Outline each Trypanosoma brucei.
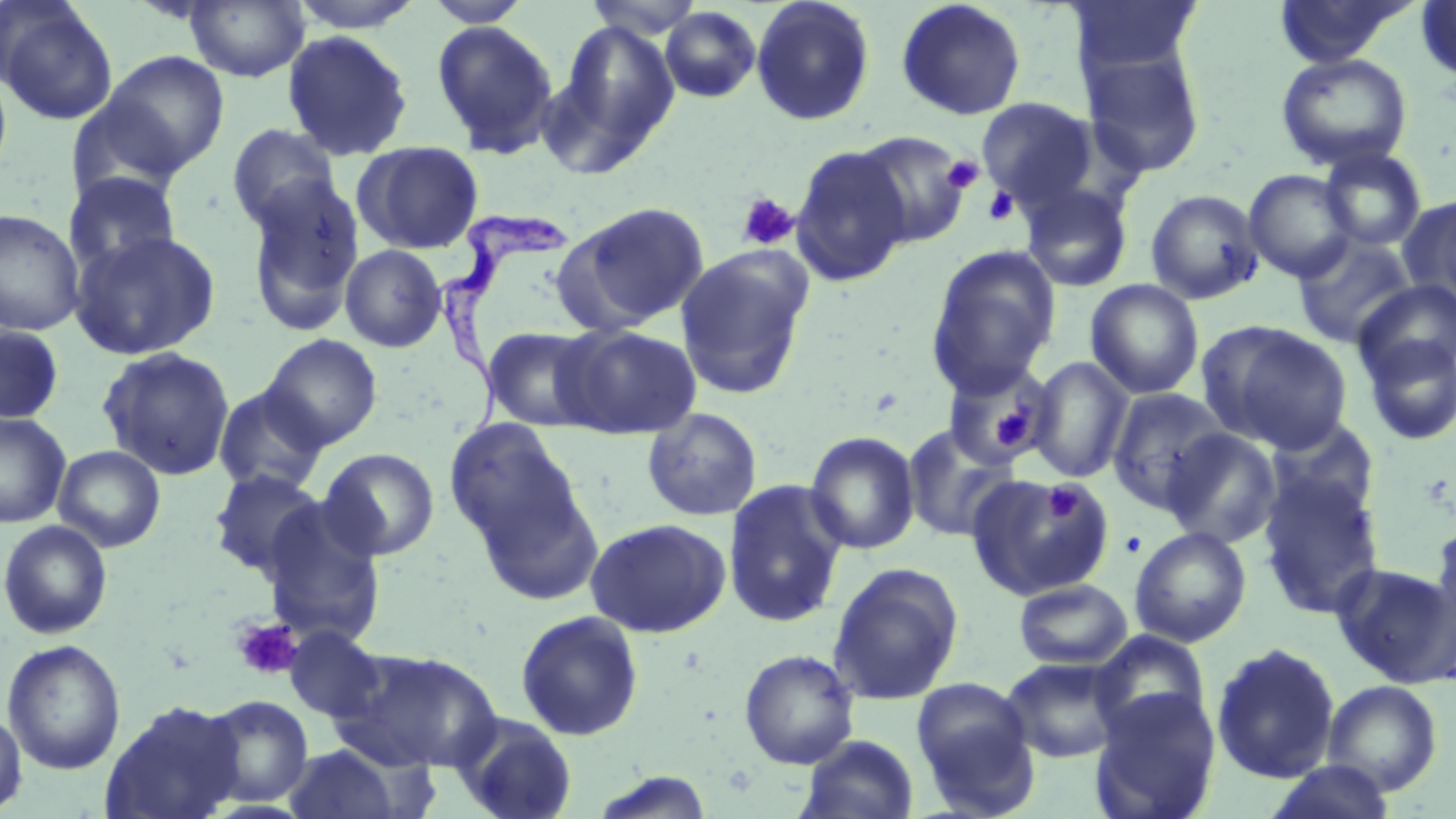
Approximate bounding boxes as (x1,y1)-(x2,y2) corner pairs in pixels.
Trypanosoma brucei: (430,209)-(570,440).

slide-level diagnosis = Trypanosoma brucei
magnification = 1000x
stain = May-Grünwald-Giemsa
uninfected red blood cell locations = approximate bounding boxes as (x1,y1)-(x2,y2) corner pairs in pixels: (287,0)-(427,33), (582,0)-(710,40), (750,0)-(876,126), (1065,0)-(1204,79), (1273,0)-(1415,69), (184,1)-(310,82), (423,1)-(532,28), (895,1)-(1027,121), (1414,1)-(1456,85), (0,2)-(119,125), (660,6)-(761,103), (541,18)-(682,174), (431,20)-(560,158), (282,30)-(413,162), (1079,45)-(1207,178), (99,50)-(229,177), (1276,52)-(1413,172), (0,61)-(14,188), (976,97)-(1100,209), (226,123)-(342,233), (852,130)-(971,249), (354,141)-(484,254), (790,144)-(912,286), (1318,147)-(1427,251), (1244,169)-(1357,281), (62,171)-(181,276), (244,176)-(365,335), (1020,183)-(1133,293), (1145,189)-(1265,305), (1401,195)-(1456,309), (561,201)-(711,331), (0,208)-(85,336), (69,228)-(221,361), (1293,233)-(1417,348), (339,244)-(447,352), (926,244)-(1061,396), (675,248)-(812,399), (1085,279)-(1204,400), (1354,279)-(1456,384), (1197,320)-(1353,454), (0,325)-(64,425), (481,325)-(605,432), (556,325)-(701,438), (1359,333)-(1456,446), (261,334)-(383,450), (97,346)-(236,480), (1027,356)-(1134,483), (942,359)-(1054,467), (212,385)-(329,495), (1107,388)-(1230,512), (642,407)-(763,522), (0,411)-(72,528), (444,417)-(588,565), (1265,417)-(1380,524), (902,423)-(1020,543), (1161,427)-(1283,548), (804,431)-(921,555), (52,444)-(165,552), (319,447)-(440,561), (208,468)-(327,579), (966,473)-(1114,600), (1258,474)-(1386,618), (723,479)-(849,628), (258,499)-(388,648), (585,517)-(732,638), (1430,518)-(1456,646), (0,519)-(113,639), (1130,526)-(1251,647), (827,562)-(964,705), (1331,562)-(1455,686), (1013,579)-(1133,669), (514,610)-(645,742), (284,626)-(387,723), (1090,630)-(1211,738), (2,638)-(126,775), (1211,642)-(1340,783), (331,646)-(502,772), (739,648)-(859,769), (1001,656)-(1126,763), (910,677)-(1039,814), (1323,680)-(1442,795), (1090,689)-(1220,819), (200,695)-(314,807), (99,699)-(246,819), (0,710)-(27,815), (453,713)-(579,819), (796,734)-(920,819), (284,744)-(404,818), (1265,760)-(1398,819)
preparation = thin blood film
platelet locations = approximate bounding boxes as (x1,y1)-(x2,y2) corner pairs in pixels: (943,156)-(983,194), (983,186)-(1019,226), (737,193)-(799,251), (993,403)-(1036,447), (1045,483)-(1082,525), (1119,531)-(1146,558), (230,617)-(303,681)
image size = 1456×819 pixels
modality = optical microscopy
field of view = single